Give the position of every Plasmodium parasite visible.
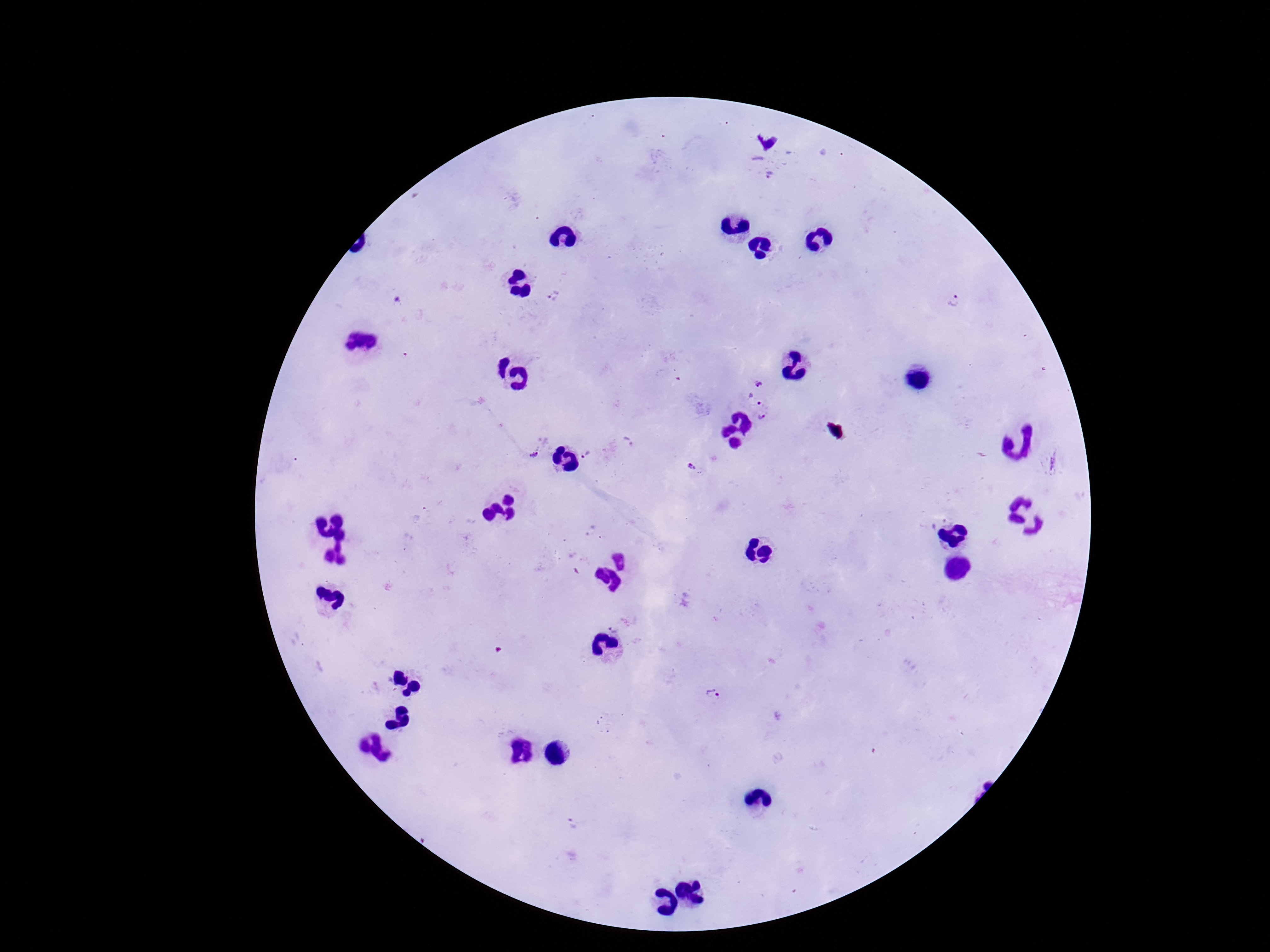

Approximate centers as {x, y} in pixels.
Plasmodium parasites: {772, 174}, {553, 297}, {398, 300}, {958, 300}, {758, 383}, {753, 399}, {764, 414}, {629, 441}, {534, 450}, {588, 454}, {1051, 462}, {693, 467}, {712, 697}, {573, 824}.

{
  "capture": "smartphone camera through the microscope eyepiece",
  "stain": "Giemsa",
  "image_size": "1270×952 pixels",
  "patient_malaria_status": "positive",
  "magnification": "100x",
  "field_of_view": "one from this slide",
  "preparation": "thick blood smear"
}